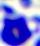

identification = white blood cell
magnification = 400x
modality = micrograph